Locate every blood parasite and identify its species.
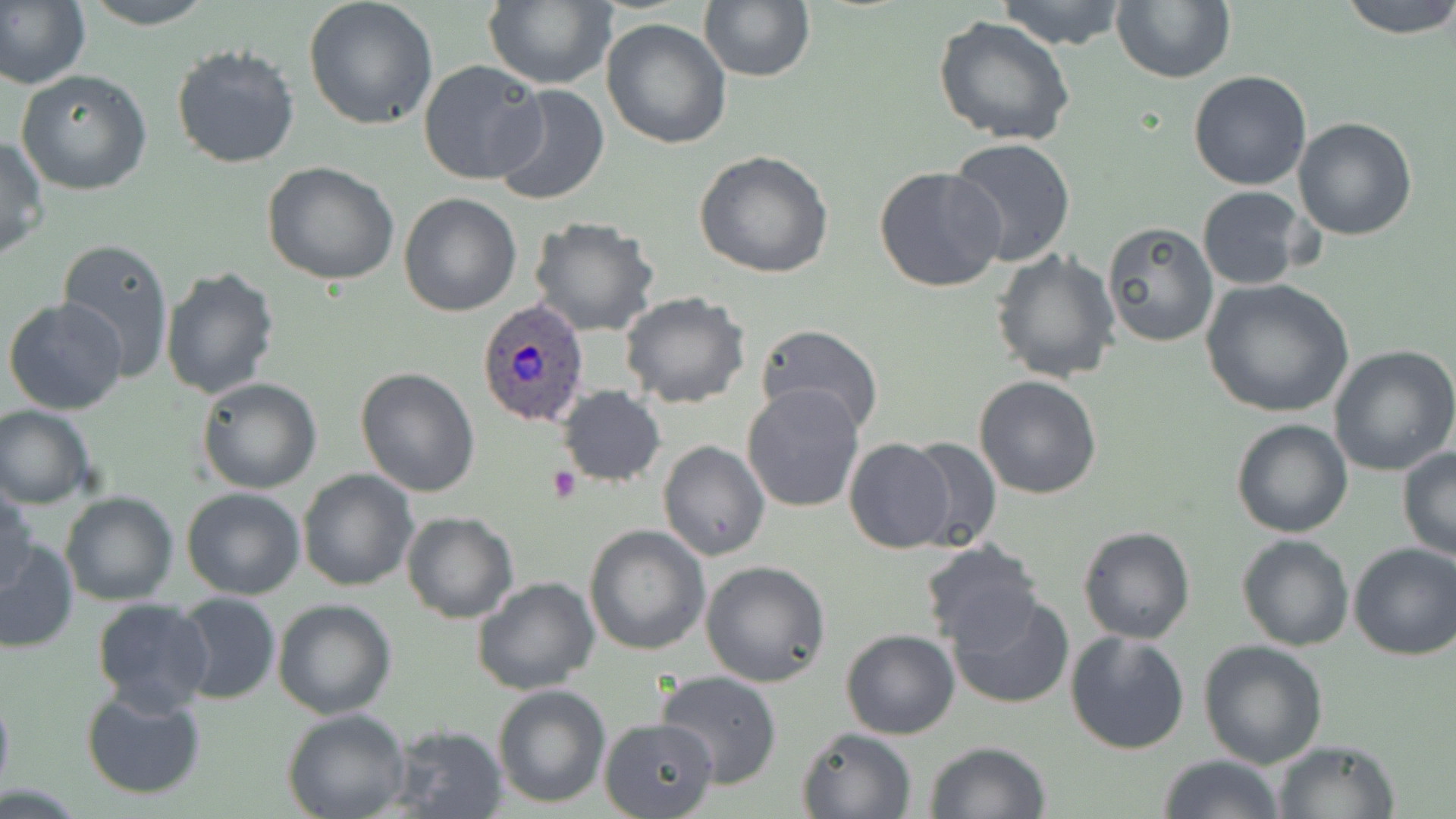
Approximate bounding boxes as (x1,y1)-(x2,y2) corner pairs in pixels.
Plasmodium ovale-infected red blood cells: (478,299)-(590,428).
No Plasmodium falciparum, Plasmodium malariae, Plasmodium vivax, Babesia divergens, or Trypanosoma brucei observed.

Summary:
  - Platelet locations: (548,464)-(583,505)
  - Uninfected red blood cell locations: (0,0)-(91,93), (78,0)-(218,29), (484,0)-(618,91), (699,0)-(814,82), (995,0)-(1130,50), (1112,0)-(1237,84), (1338,0)-(1456,39), (303,2)-(439,131), (933,15)-(1076,147), (600,19)-(732,150), (171,42)-(301,170), (419,59)-(547,187), (15,69)-(152,195), (1187,70)-(1312,190), (490,83)-(611,207), (1292,118)-(1418,240), (0,136)-(48,261), (946,138)-(1077,265), (694,151)-(836,279), (263,162)-(401,286), (873,166)-(1006,295), (1196,185)-(1312,290), (399,191)-(522,316), (528,216)-(660,337), (1100,222)-(1220,348), (56,237)-(175,381), (991,247)-(1120,383), (159,264)-(281,399), (1199,277)-(1355,418), (620,292)-(750,407), (2,299)-(130,417), (756,324)-(883,438), (1328,345)-(1456,476), (354,367)-(480,498), (974,374)-(1104,499), (196,377)-(323,494), (742,383)-(865,514), (557,385)-(666,487), (0,404)-(95,510), (1230,418)-(1355,538), (903,435)-(1004,552), (844,438)-(957,554), (658,440)-(770,562), (1396,447)-(1456,562), (297,469)-(417,591), (0,481)-(37,595), (181,486)-(306,600), (60,490)-(177,605), (400,510)-(520,623), (583,524)-(711,655), (1077,525)-(1197,644), (1236,534)-(1354,651), (0,537)-(77,654), (918,542)-(1045,652), (1347,542)-(1455,660), (700,561)-(831,687), (471,577)-(601,696), (946,588)-(1076,711), (172,593)-(281,705), (92,597)-(214,714), (272,598)-(397,719), (841,629)-(961,740), (1063,630)-(1191,755), (1197,639)-(1329,770), (656,669)-(783,789), (492,684)-(610,808), (0,685)-(13,802), (80,687)-(207,800), (283,708)-(412,819), (599,716)-(720,819), (386,724)-(510,819), (796,727)-(916,819), (1270,739)-(1400,819), (923,740)-(1053,819), (1158,753)-(1285,819)
  - Slide-level diagnosis: Plasmodium ovale
  - Field of view: single
  - Stain: May-Grünwald-Giemsa
  - Preparation: thin blood smear
  - Modality: light microscopy
  - Image size: 1456×819 pixels
  - Magnification: 1000x